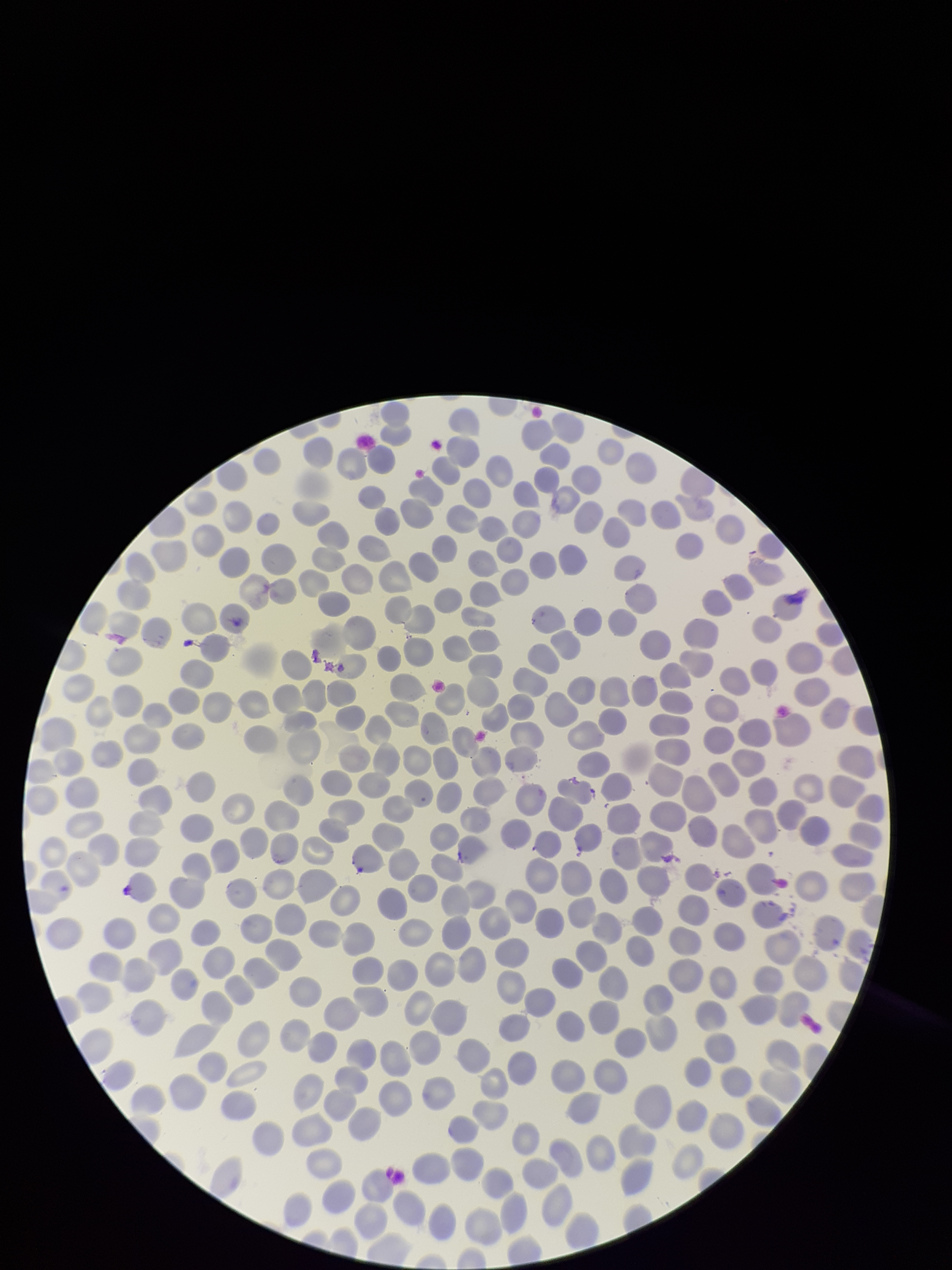

species reported for this patient = Plasmodium vivax
parasitized red blood cell count = 0
capture = smartphone photograph through the microscope eyepiece
preparation = thin
image size = 952×1270 pixels
red blood cell count = 351
field of view = one from this slide
parasitized red blood cells = none identified
patient malaria status = positive
stain = Giemsa